Describe the morphology of the erythrocytes.
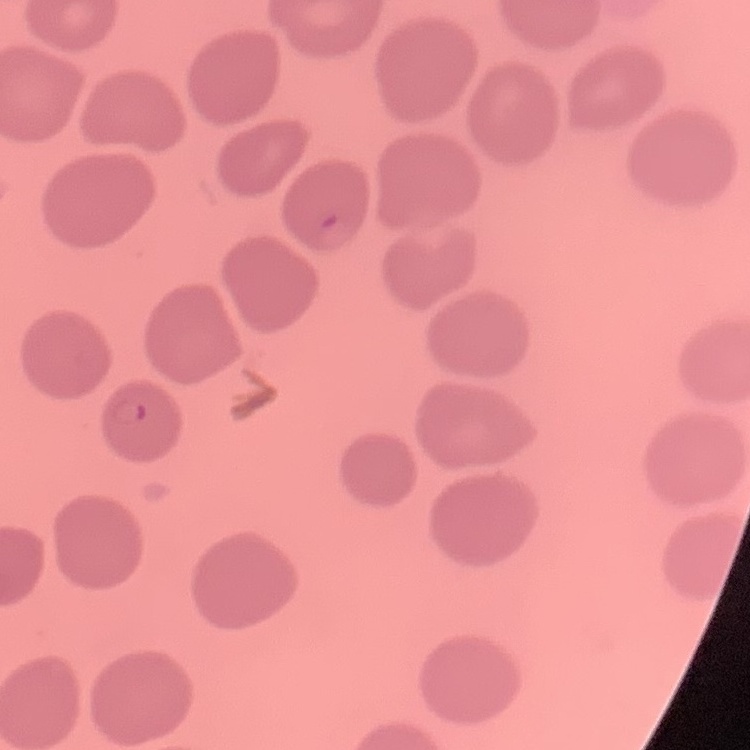
No rouleaux formation.

preparation: thin blood film
stain: Field's or Giemsa
image_type: one tile cut from a larger photomicrograph